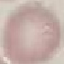
result: no malaria parasites seen
capture: smartphone camera at the microscope eyepiece
preparation: thin blood smear
image_type: cell patch, automatically extracted from a larger field of view and resized to 64 × 64 pixels
stain: Giemsa